Assess the morphology of the erythrocytes.
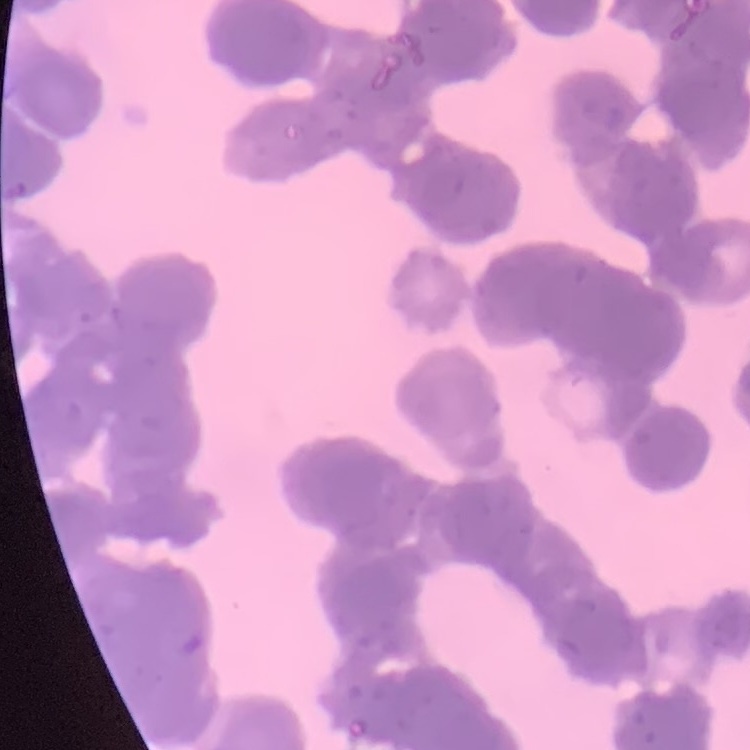
Rouleaux formation.

stain: Field's or Giemsa
image_type: square crop of a larger photomicrograph
preparation: thin blood film